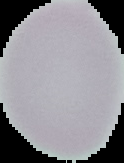
Result: no Plasmodium parasites detected. Image is 124×163 pixels. Segmented cell region on a black background. From a thin blood film.